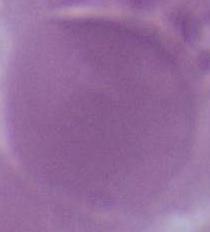

Photomicrograph. 1000x magnification. An erythrocyte is seen.